Outline each Plasmodium falciparum-infected red blood cell.
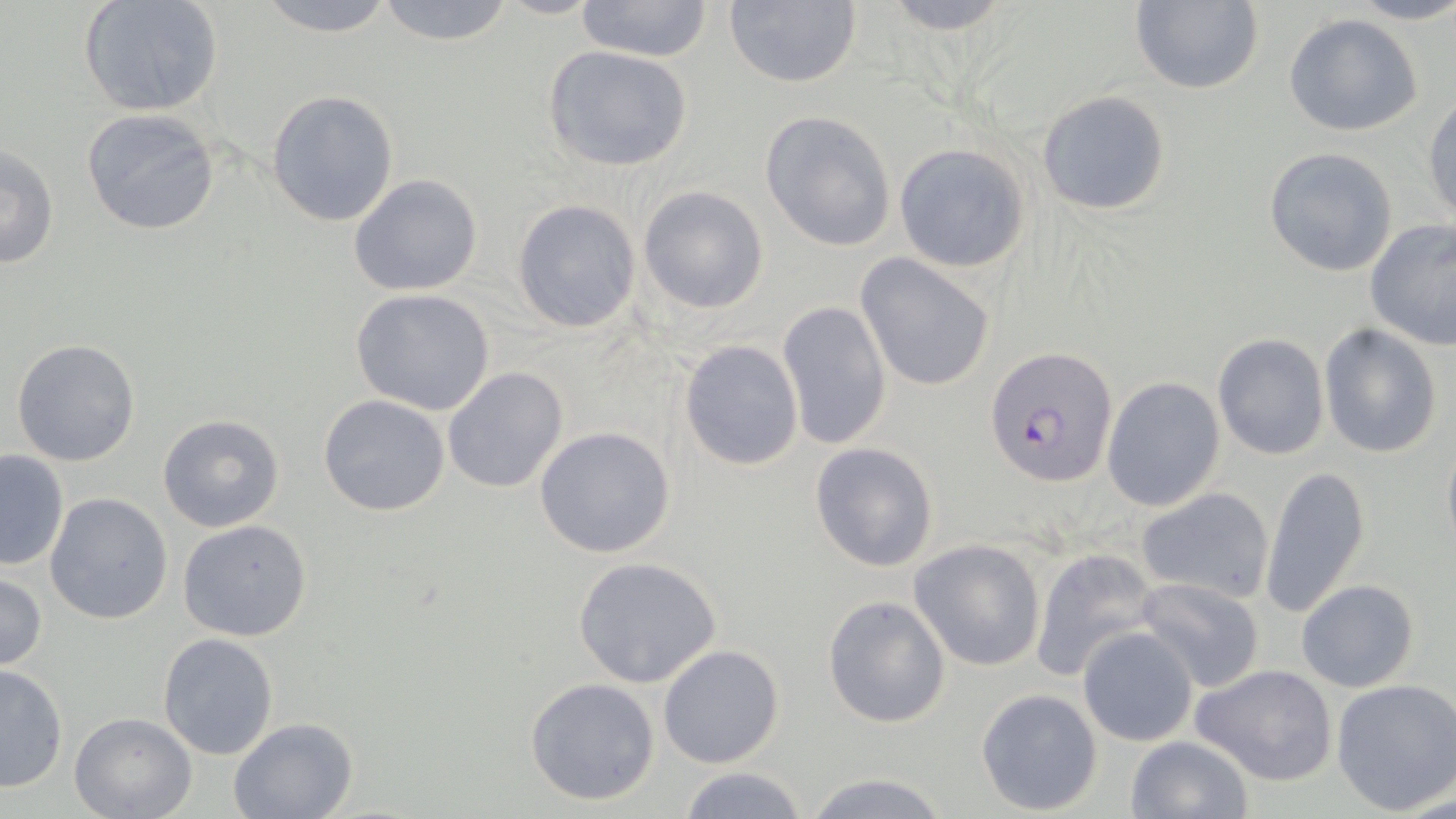

Approximate bounding boxes as [x1, y1, x2, y2] in pixels.
Plasmodium falciparum-infected red blood cells: [986, 349, 1117, 487].

Uninfected red blood cell locations: [78, 0, 225, 118], [249, 0, 403, 36], [722, 0, 863, 89], [869, 0, 1022, 32], [1343, 0, 1456, 25], [372, 1, 520, 46], [578, 1, 710, 61], [1129, 1, 1265, 94], [1283, 13, 1424, 137], [542, 44, 696, 173], [265, 90, 400, 227], [1037, 91, 1171, 215], [1424, 94, 1456, 226], [79, 108, 223, 237], [759, 111, 896, 252], [1, 142, 60, 271], [891, 142, 1031, 273], [1264, 146, 1397, 276], [347, 173, 483, 296], [637, 185, 769, 314], [512, 198, 642, 334], [1364, 219, 1456, 351], [857, 255, 996, 392], [351, 288, 495, 416], [776, 300, 893, 452], [1319, 324, 1444, 460], [1213, 333, 1329, 461], [10, 338, 142, 468], [679, 339, 804, 470], [442, 367, 569, 495], [1102, 376, 1225, 511], [319, 394, 452, 516], [157, 413, 286, 532], [534, 425, 678, 560], [1441, 435, 1456, 563], [810, 441, 939, 572], [0, 449, 69, 571], [1260, 464, 1372, 621], [1136, 486, 1275, 604], [44, 492, 173, 625], [177, 521, 314, 642], [909, 539, 1046, 671], [1030, 546, 1162, 684], [572, 556, 723, 689], [0, 571, 48, 672], [1133, 577, 1267, 695], [1296, 578, 1419, 693], [822, 594, 951, 728], [1077, 627, 1198, 746], [156, 632, 280, 760], [658, 643, 786, 769], [0, 663, 68, 793], [1191, 663, 1339, 786], [523, 677, 663, 807], [1331, 678, 1456, 814], [976, 688, 1104, 816], [69, 712, 196, 819], [228, 717, 359, 819], [1125, 735, 1252, 819], [676, 764, 810, 819], [801, 770, 955, 819]. Slide-level diagnosis: Plasmodium falciparum. 1000x magnification. One field of a larger specimen. Light microscopy. Image is 1456×819 pixels. May-Grünwald-Giemsa-stained preparation. Thin blood smear.